Give the position of every malaria parasite.
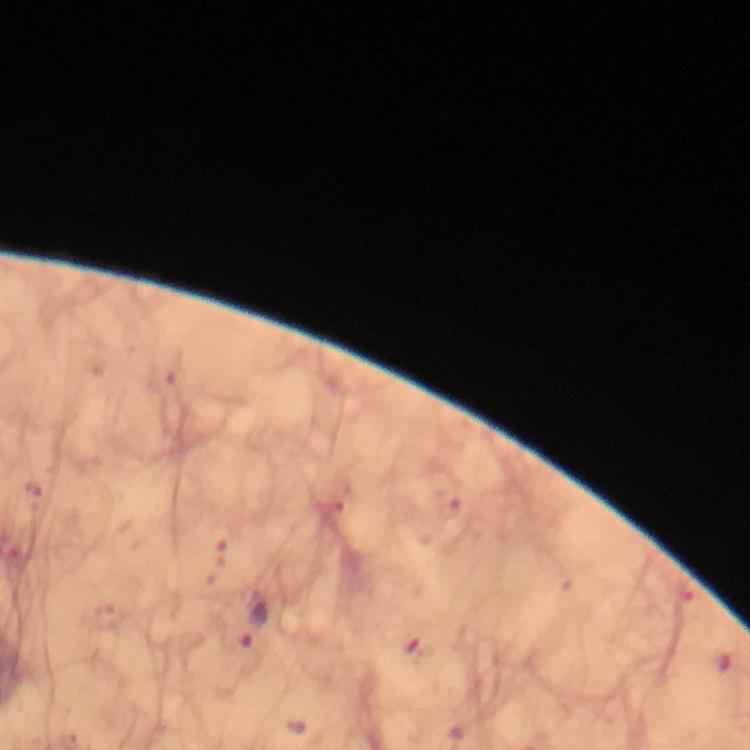

Approximate object centers, in pixels from the top-left corner.
Malaria parasites: (x=253, y=625).

immersion oil = used
magnification = 100x
image size = 750×750 pixels
stain = Giemsa
capture = smartphone mounted on the microscope
cropped from = one field of view
preparation = thick blood film
context = from a diagnostic examination for malaria